Evaluate for malaria.
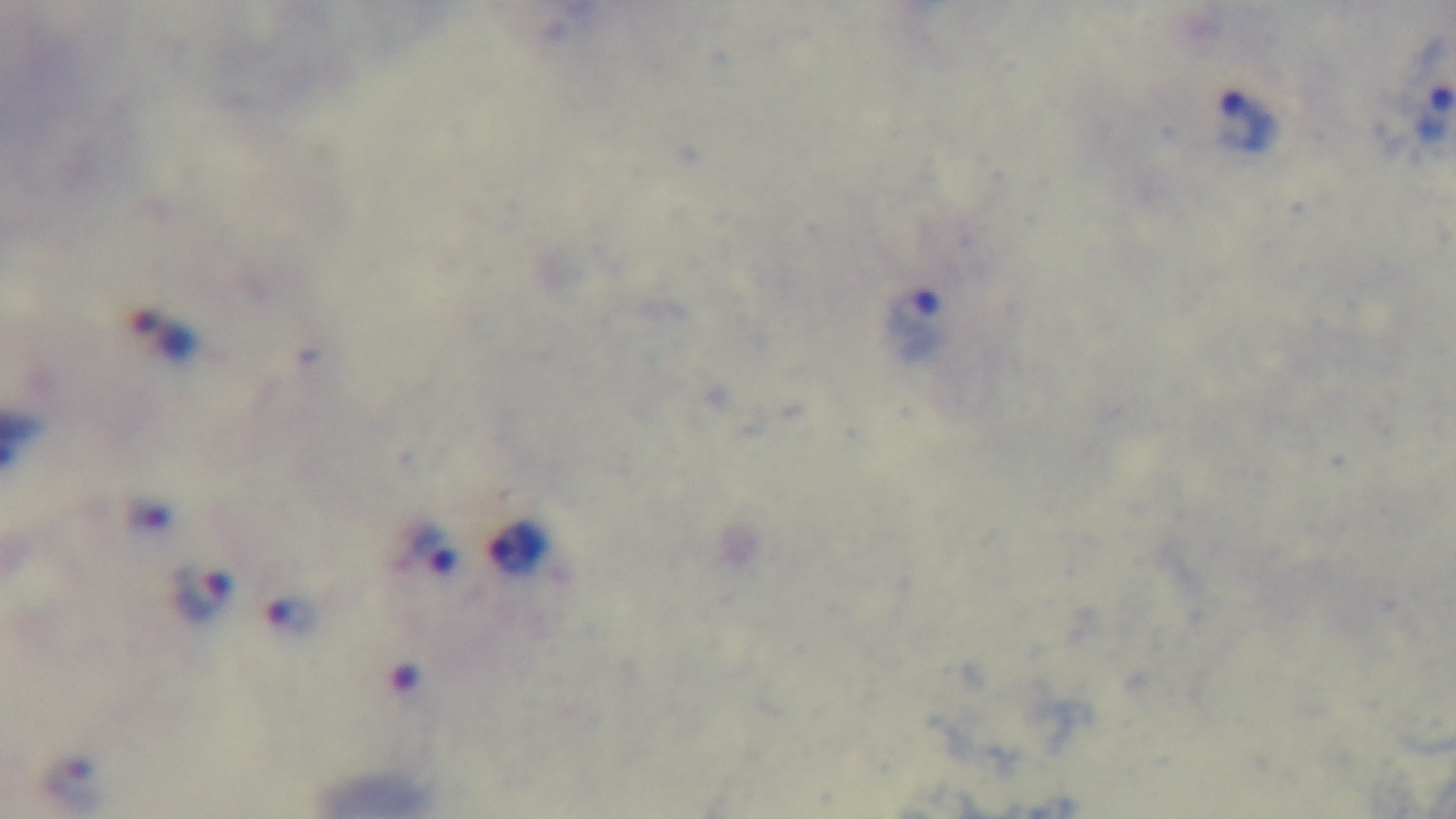
It is infected.

stain = Giemsa
modality = light microscopy
preparation = thick smear
capture = mounted 4K digital camera
objective = 100x oil immersion
field of view = one from the slide